Assess the morphology of the red blood cells.
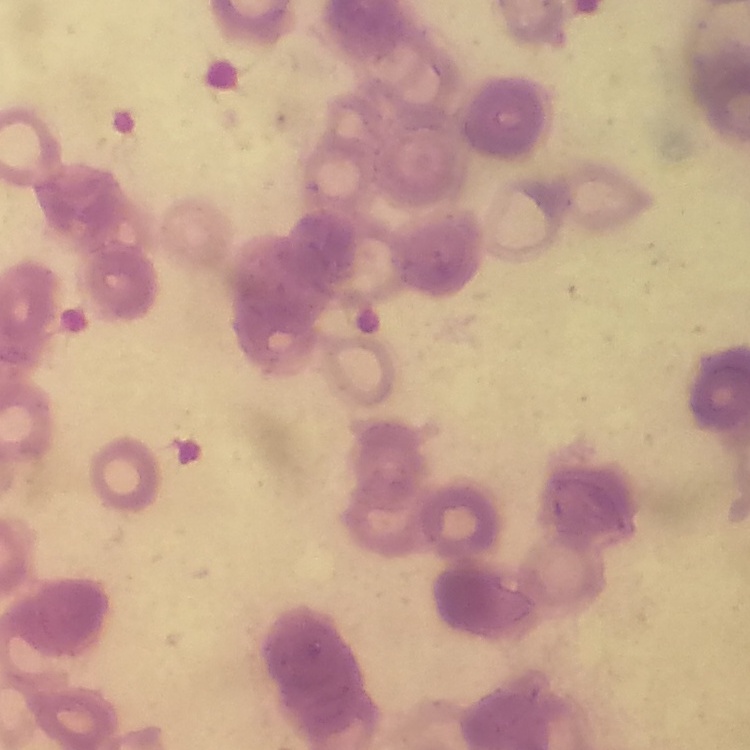

Rouleaux formation.

Stained with either Field's or Giemsa. One tile cut from a larger photomicrograph. Thin peripheral smear.